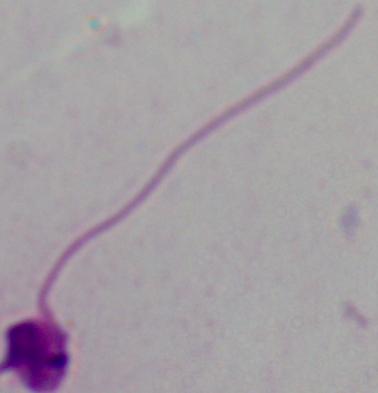
Summary:
  - Modality: micrograph
  - Magnification: 1000x
  - Identification: Leishmania